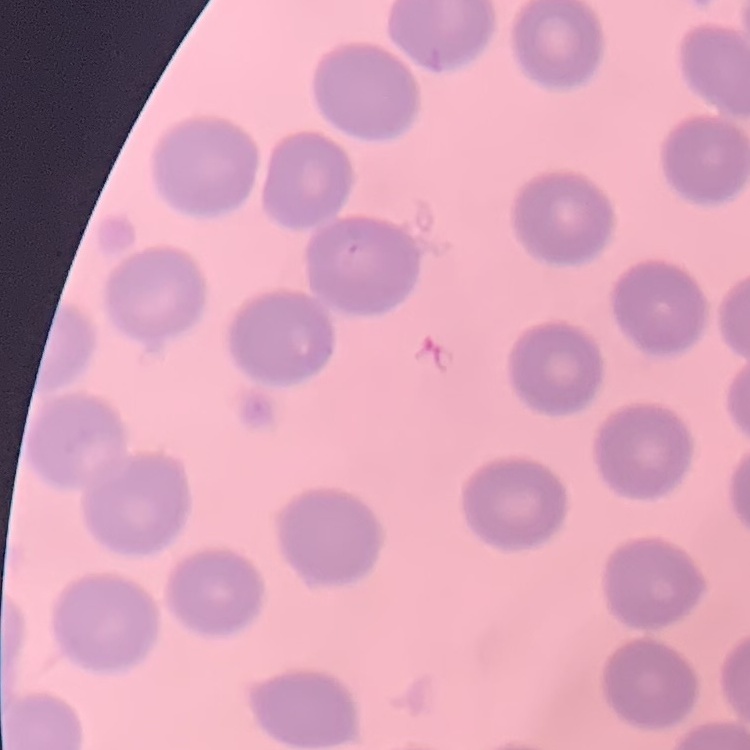

Summary:
  - Erythrocyte morphology: no rouleaux formation
  - Preparation: thin blood film
  - Image type: one tile cut from a larger photomicrograph
  - Stain: Field's or Giemsa